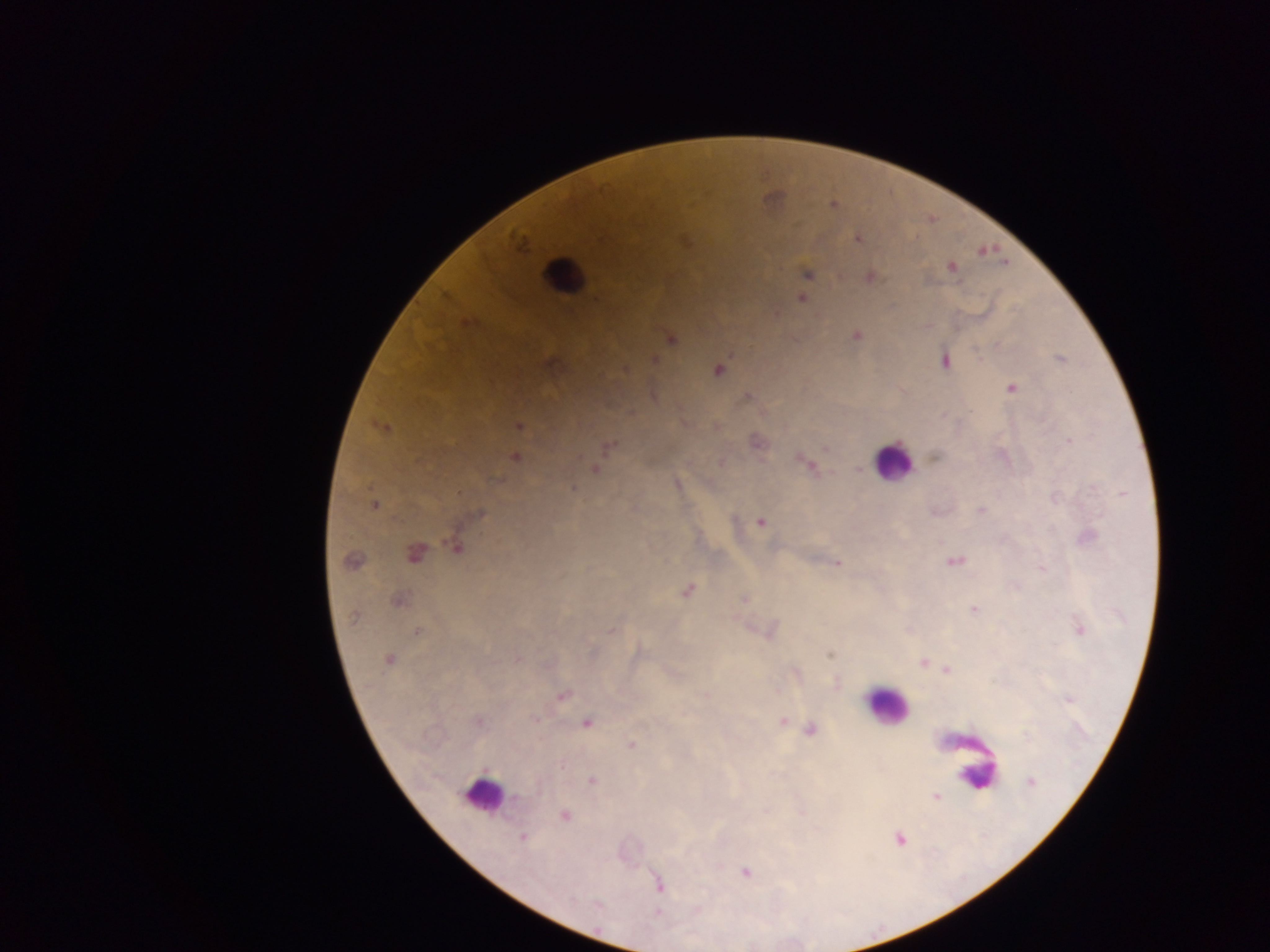
malaria parasite locations = approximate centers as [x, y] in pixels: [833, 205], [858, 238], [519, 240], [981, 251], [951, 267], [806, 273], [870, 276], [801, 298], [467, 323], [856, 336], [670, 338], [1060, 359], [653, 360], [944, 360], [624, 370], [717, 370], [1010, 387], [747, 395], [518, 426], [381, 427], [756, 441], [1068, 441], [607, 446], [825, 447], [935, 456], [514, 457], [721, 463], [805, 464], [595, 469], [676, 484], [574, 488], [373, 505], [981, 511], [478, 514], [760, 521], [1087, 537], [456, 545], [413, 553], [954, 561], [351, 562], [836, 563], [1042, 567], [687, 590], [745, 599], [398, 600], [973, 608], [1078, 628], [612, 629], [769, 630], [417, 631], [828, 655], [388, 660], [923, 662], [948, 670], [795, 673], [836, 683], [561, 694], [704, 695], [1069, 699], [478, 721], [782, 722], [585, 723], [809, 730], [631, 746], [591, 781], [1030, 782], [935, 796], [564, 815], [522, 837], [899, 839], [744, 872], [658, 884]
country = Ghana
leukocyte locations = approximate centers as [x, y] in pixels: [563, 276], [892, 461], [886, 706], [976, 768], [482, 795]
preparation = thick blood film
field of view = single
image size = 1270×952 pixels
capture = mobile-phone photograph through a microscope